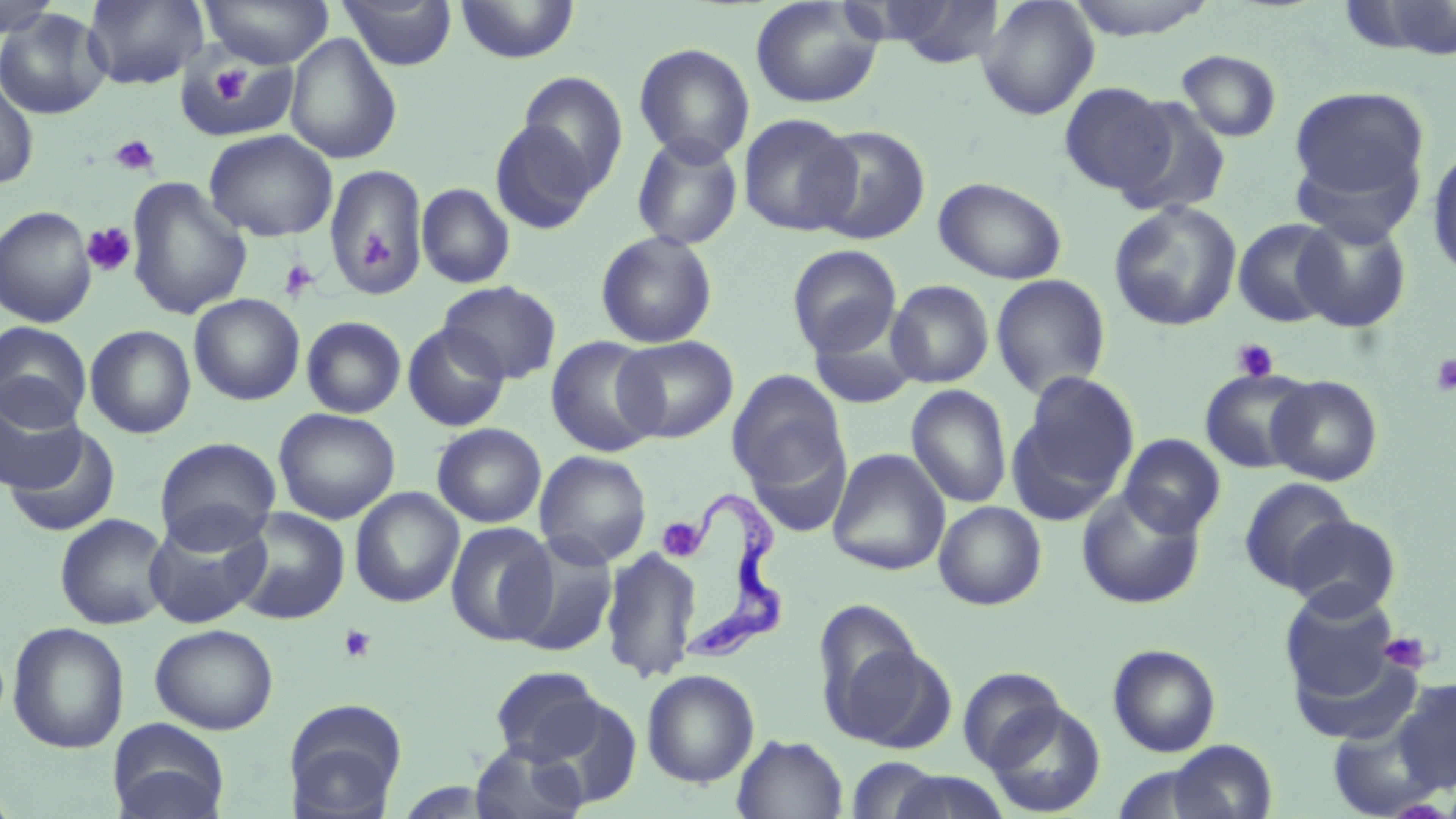
Summary:
  - Coordinate format: approximate bounding boxes as named x1/y1/x2/y2 corners in pixels
  - Trypanosoma brucei locations: (x1=693, y1=496, x2=787, y2=663)
  - Platelet locations: (x1=210, y1=65, x2=250, y2=106), (x1=110, y1=134, x2=160, y2=177), (x1=81, y1=222, x2=137, y2=276), (x1=359, y1=227, x2=393, y2=272), (x1=278, y1=258, x2=320, y2=301), (x1=1232, y1=338, x2=1279, y2=382), (x1=1429, y1=353, x2=1456, y2=397), (x1=657, y1=517, x2=705, y2=561), (x1=339, y1=624, x2=378, y2=663), (x1=1378, y1=631, x2=1433, y2=675)
  - Uninfected red blood cell locations: (x1=81, y1=0, x2=210, y2=90), (x1=199, y1=0, x2=334, y2=68), (x1=337, y1=0, x2=458, y2=71), (x1=456, y1=0, x2=579, y2=64), (x1=877, y1=0, x2=1007, y2=68), (x1=976, y1=0, x2=1100, y2=120), (x1=1063, y1=0, x2=1221, y2=40), (x1=0, y1=1, x2=63, y2=38), (x1=749, y1=1, x2=883, y2=109), (x1=1344, y1=2, x2=1456, y2=59), (x1=0, y1=8, x2=112, y2=120), (x1=285, y1=33, x2=402, y2=164), (x1=633, y1=42, x2=755, y2=164), (x1=1176, y1=49, x2=1283, y2=142), (x1=181, y1=56, x2=290, y2=139), (x1=516, y1=72, x2=628, y2=196), (x1=0, y1=75, x2=39, y2=190), (x1=1057, y1=82, x2=1175, y2=195), (x1=1289, y1=85, x2=1431, y2=211), (x1=1114, y1=97, x2=1233, y2=218), (x1=738, y1=113, x2=861, y2=235), (x1=489, y1=118, x2=600, y2=235), (x1=810, y1=124, x2=932, y2=245), (x1=204, y1=128, x2=338, y2=242), (x1=631, y1=133, x2=744, y2=251), (x1=1426, y1=144, x2=1456, y2=281), (x1=323, y1=163, x2=428, y2=298), (x1=933, y1=176, x2=1068, y2=284), (x1=124, y1=177, x2=252, y2=320), (x1=416, y1=182, x2=515, y2=289), (x1=1108, y1=200, x2=1243, y2=332), (x1=1, y1=206, x2=98, y2=327), (x1=1293, y1=215, x2=1412, y2=332), (x1=1232, y1=218, x2=1344, y2=327), (x1=594, y1=230, x2=718, y2=349), (x1=786, y1=244, x2=902, y2=359), (x1=990, y1=274, x2=1112, y2=399), (x1=886, y1=279, x2=994, y2=388), (x1=437, y1=280, x2=562, y2=384), (x1=189, y1=293, x2=306, y2=406), (x1=301, y1=315, x2=407, y2=419), (x1=808, y1=318, x2=922, y2=410), (x1=0, y1=321, x2=92, y2=429), (x1=402, y1=323, x2=510, y2=432), (x1=84, y1=324, x2=196, y2=439), (x1=614, y1=336, x2=738, y2=443), (x1=546, y1=337, x2=663, y2=457), (x1=1199, y1=368, x2=1318, y2=474), (x1=727, y1=369, x2=848, y2=488), (x1=1014, y1=370, x2=1140, y2=512), (x1=1266, y1=375, x2=1383, y2=486), (x1=906, y1=385, x2=1012, y2=509), (x1=0, y1=387, x2=87, y2=493), (x1=273, y1=408, x2=400, y2=524), (x1=431, y1=423, x2=547, y2=528), (x1=4, y1=425, x2=121, y2=537), (x1=1119, y1=433, x2=1226, y2=537), (x1=154, y1=437, x2=281, y2=551), (x1=746, y1=437, x2=851, y2=538), (x1=827, y1=448, x2=950, y2=576), (x1=535, y1=450, x2=652, y2=568), (x1=1238, y1=477, x2=1356, y2=592), (x1=350, y1=488, x2=464, y2=607), (x1=1076, y1=489, x2=1206, y2=609), (x1=933, y1=501, x2=1047, y2=610), (x1=229, y1=506, x2=351, y2=625), (x1=54, y1=513, x2=171, y2=630), (x1=144, y1=515, x2=270, y2=629), (x1=1283, y1=515, x2=1401, y2=618), (x1=445, y1=521, x2=557, y2=646), (x1=509, y1=535, x2=619, y2=658), (x1=601, y1=546, x2=702, y2=683), (x1=1280, y1=587, x2=1408, y2=716), (x1=813, y1=601, x2=933, y2=742), (x1=7, y1=622, x2=129, y2=754), (x1=150, y1=623, x2=279, y2=734), (x1=1107, y1=644, x2=1222, y2=757), (x1=1291, y1=647, x2=1427, y2=746), (x1=489, y1=666, x2=607, y2=765), (x1=958, y1=667, x2=1069, y2=772), (x1=642, y1=669, x2=760, y2=788), (x1=1389, y1=678, x2=1456, y2=794), (x1=532, y1=696, x2=643, y2=810), (x1=283, y1=698, x2=408, y2=817), (x1=984, y1=701, x2=1106, y2=817), (x1=108, y1=718, x2=230, y2=819), (x1=732, y1=734, x2=848, y2=818), (x1=1165, y1=740, x2=1277, y2=819), (x1=470, y1=742, x2=588, y2=819), (x1=844, y1=757, x2=945, y2=819), (x1=885, y1=770, x2=1012, y2=818)
  - Slide-level diagnosis: Trypanosoma brucei
  - Image size: 1456×819 pixels
  - Stain: May-Grünwald-Giemsa
  - Field of view: one of a larger specimen
  - Magnification: 1000x
  - Modality: light microscopy
  - Preparation: thin blood film